Name the parasite shown.
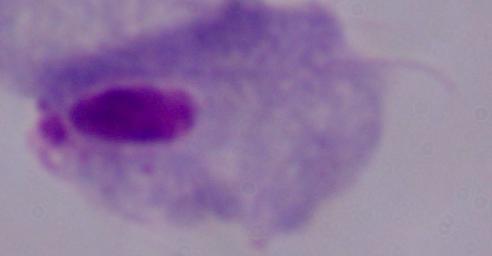
This is a trichomonad.

1000x magnification. Micrograph.